Give the position of every Plasmodium parasite.
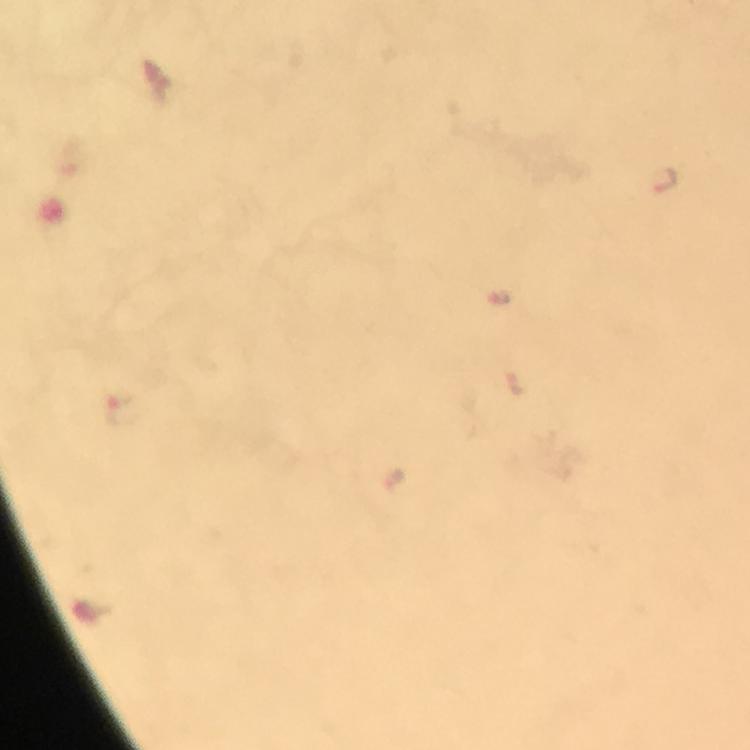
Approximate centers as [x, y] in pixels.
Plasmodium parasites: [123, 407].

Giemsa-stained preparation. Immersion oil applied. Image is 750×750 pixels. Cropped region of a single field of view. Smartphone photograph taken through a microscope. Thick blood film. From a malaria diagnostic workup. At 100x magnification.